Assess this cell for malaria.
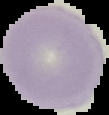
It is uninfected.

From a thin blood smear. Cell region segmented out of the field of view; the surrounding area is masked to black. Image is 109×115 pixels.